State which parasite is depicted.
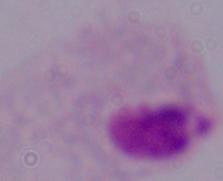
A trichomonad.

modality = micrograph
magnification = 1000x